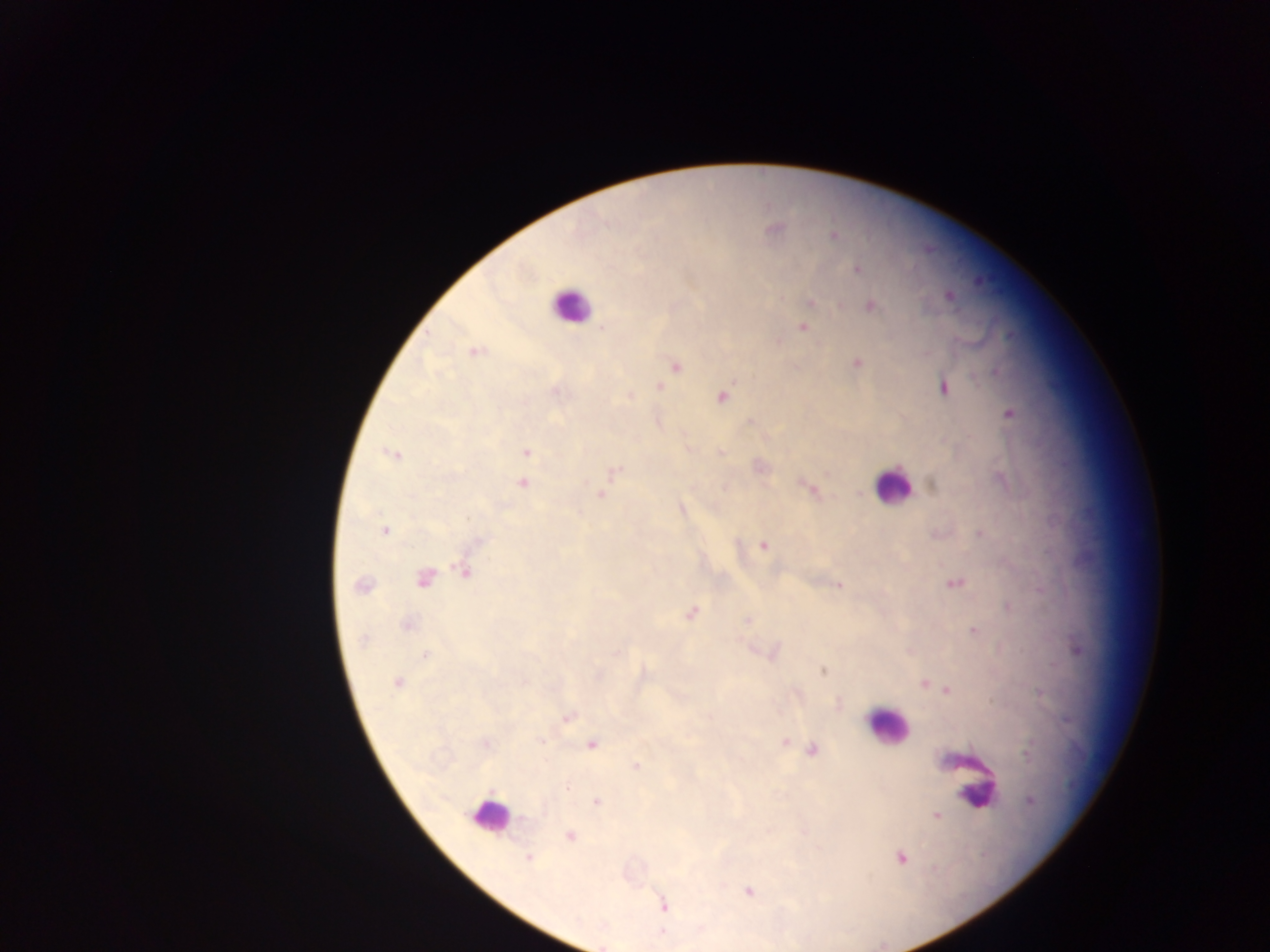

Approximate centers as {x, y} in pixels.
Summary:
  - Malaria parasite locations: {773, 231}, {834, 236}, {858, 270}, {949, 296}, {811, 302}, {871, 306}, {803, 327}, {602, 328}, {474, 351}, {857, 363}, {676, 367}, {996, 372}, {659, 387}, {943, 388}, {557, 391}, {630, 396}, {722, 397}, {1010, 414}, {750, 421}, {526, 452}, {721, 452}, {392, 454}, {616, 470}, {522, 483}, {809, 489}, {601, 494}, {385, 531}, {980, 533}, {479, 542}, {764, 546}, {465, 573}, {424, 578}, {955, 583}, {361, 585}, {839, 586}, {691, 613}, {747, 621}, {408, 624}, {974, 630}, {364, 640}, {1077, 649}, {425, 655}, {823, 671}, {397, 683}, {924, 683}, {948, 690}, {568, 718}, {541, 741}, {785, 741}, {487, 744}, {591, 745}, {813, 750}, {1027, 753}, {636, 766}, {566, 787}, {1030, 801}, {597, 802}, {937, 815}, {570, 836}, {901, 858}, {528, 859}, {748, 892}, {663, 906}
  - Leukocyte locations: {570, 305}, {892, 485}, {886, 727}, {975, 792}, {489, 815}
  - Field of view: single
  - Image size: 1270×952 pixels
  - Capture: mobile-phone photograph through a microscope
  - Country: Ghana
  - Preparation: thick blood film